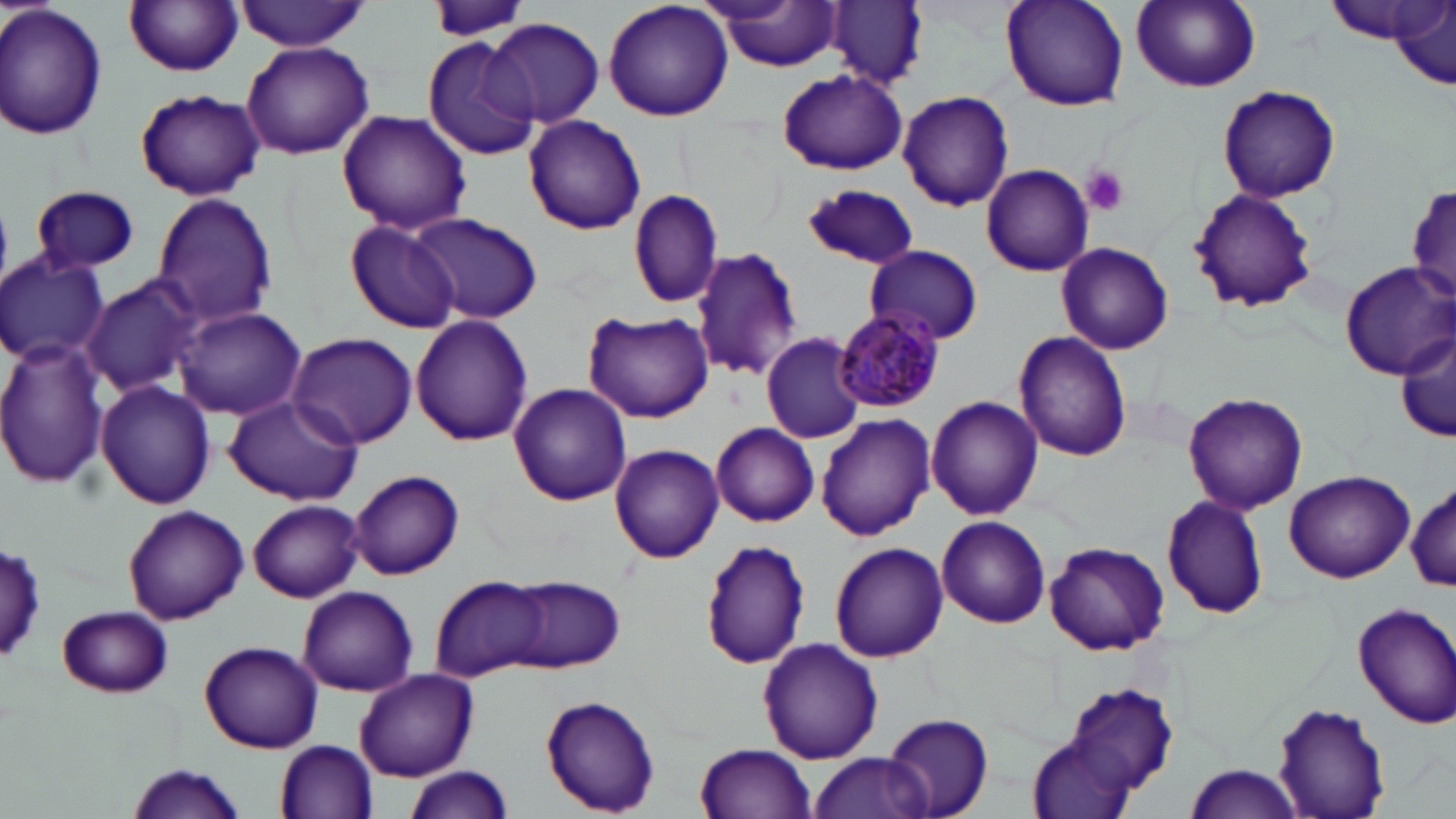

Summary:
  - Coordinate format: approximate bounding boxes as named x1/y1/x2/y2 corners in pixels
  - Platelet locations: (x1=1082, y1=166, x2=1129, y2=216)
  - Uninfected red blood cell locations: (x1=424, y1=0, x2=531, y2=44), (x1=603, y1=0, x2=735, y2=122), (x1=999, y1=0, x2=1130, y2=113), (x1=1129, y1=0, x2=1261, y2=92), (x1=125, y1=1, x2=243, y2=77), (x1=707, y1=1, x2=843, y2=71), (x1=1322, y1=1, x2=1441, y2=43), (x1=236, y1=2, x2=371, y2=52), (x1=828, y1=2, x2=927, y2=86), (x1=0, y1=3, x2=106, y2=141), (x1=1393, y1=3, x2=1455, y2=91), (x1=485, y1=17, x2=605, y2=128), (x1=423, y1=38, x2=539, y2=161), (x1=240, y1=42, x2=374, y2=160), (x1=775, y1=67, x2=909, y2=177), (x1=1216, y1=84, x2=1342, y2=204), (x1=135, y1=89, x2=265, y2=201), (x1=896, y1=91, x2=1016, y2=212), (x1=336, y1=109, x2=472, y2=236), (x1=523, y1=115, x2=647, y2=235), (x1=980, y1=164, x2=1095, y2=276), (x1=1406, y1=183, x2=1455, y2=306), (x1=29, y1=184, x2=139, y2=275), (x1=803, y1=184, x2=917, y2=271), (x1=1186, y1=188, x2=1320, y2=315), (x1=628, y1=189, x2=725, y2=308), (x1=151, y1=194, x2=278, y2=327), (x1=405, y1=213, x2=545, y2=325), (x1=345, y1=220, x2=461, y2=333), (x1=1056, y1=243, x2=1174, y2=355), (x1=864, y1=245, x2=984, y2=345), (x1=689, y1=248, x2=805, y2=381), (x1=0, y1=253, x2=108, y2=366), (x1=1339, y1=263, x2=1454, y2=378), (x1=81, y1=275, x2=202, y2=397), (x1=174, y1=306, x2=306, y2=421), (x1=583, y1=311, x2=713, y2=421), (x1=410, y1=314, x2=534, y2=446), (x1=1397, y1=327, x2=1455, y2=448), (x1=287, y1=332, x2=417, y2=449), (x1=758, y1=332, x2=868, y2=445), (x1=1013, y1=332, x2=1133, y2=464), (x1=0, y1=337, x2=110, y2=488), (x1=96, y1=381, x2=216, y2=510), (x1=508, y1=382, x2=632, y2=505), (x1=1181, y1=390, x2=1309, y2=515), (x1=222, y1=395, x2=363, y2=506), (x1=926, y1=396, x2=1044, y2=521), (x1=815, y1=415, x2=937, y2=542), (x1=711, y1=421, x2=820, y2=528), (x1=608, y1=444, x2=723, y2=563), (x1=348, y1=468, x2=465, y2=581), (x1=1283, y1=470, x2=1414, y2=584), (x1=1408, y1=480, x2=1456, y2=595), (x1=1160, y1=495, x2=1271, y2=621), (x1=247, y1=499, x2=364, y2=602), (x1=122, y1=505, x2=249, y2=624), (x1=937, y1=515, x2=1049, y2=629), (x1=700, y1=539, x2=812, y2=668), (x1=1042, y1=540, x2=1169, y2=655), (x1=829, y1=542, x2=948, y2=661), (x1=2, y1=543, x2=48, y2=665), (x1=432, y1=577, x2=550, y2=681), (x1=506, y1=577, x2=625, y2=672), (x1=299, y1=585, x2=417, y2=695), (x1=1354, y1=601, x2=1456, y2=728), (x1=58, y1=605, x2=173, y2=697), (x1=758, y1=637, x2=883, y2=764), (x1=199, y1=640, x2=323, y2=751), (x1=354, y1=668, x2=476, y2=781), (x1=1062, y1=684, x2=1181, y2=802), (x1=540, y1=696, x2=662, y2=815), (x1=1272, y1=701, x2=1392, y2=819), (x1=884, y1=713, x2=994, y2=817), (x1=1026, y1=735, x2=1137, y2=819), (x1=278, y1=739, x2=379, y2=817), (x1=695, y1=741, x2=818, y2=819), (x1=807, y1=752, x2=936, y2=819), (x1=128, y1=763, x2=248, y2=817), (x1=1183, y1=763, x2=1305, y2=819), (x1=399, y1=767, x2=515, y2=819)
  - Plasmodium malariae-infected red blood cell locations: (x1=834, y1=309, x2=944, y2=415)
  - Slide-level diagnosis: Plasmodium malariae
  - Modality: optical microscopy
  - Image size: 1456×819 pixels
  - Field of view: single
  - Magnification: 1000x
  - Preparation: thin blood film
  - Stain: May-Grünwald-Giemsa